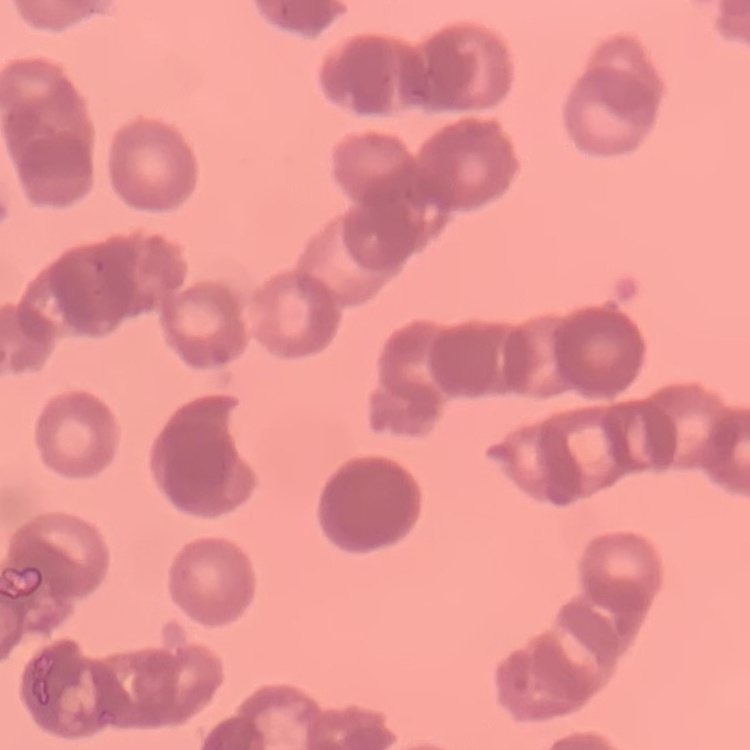
Summary:
  - Red blood cell morphology: rouleaux formation
  - Image type: square crop of a larger photomicrograph
  - Preparation: thin peripheral smear
  - Stain: Field's or Giemsa